Report the malaria status of this cell.
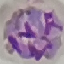

Parasitized.

Summary:
  - Preparation: thin smear
  - Capture: smartphone camera at the microscope eyepiece
  - Stain: Giemsa
  - Image type: cell patch, automatically extracted from a larger field of view and resized to 64 × 64 pixels